Name the blood parasite species.
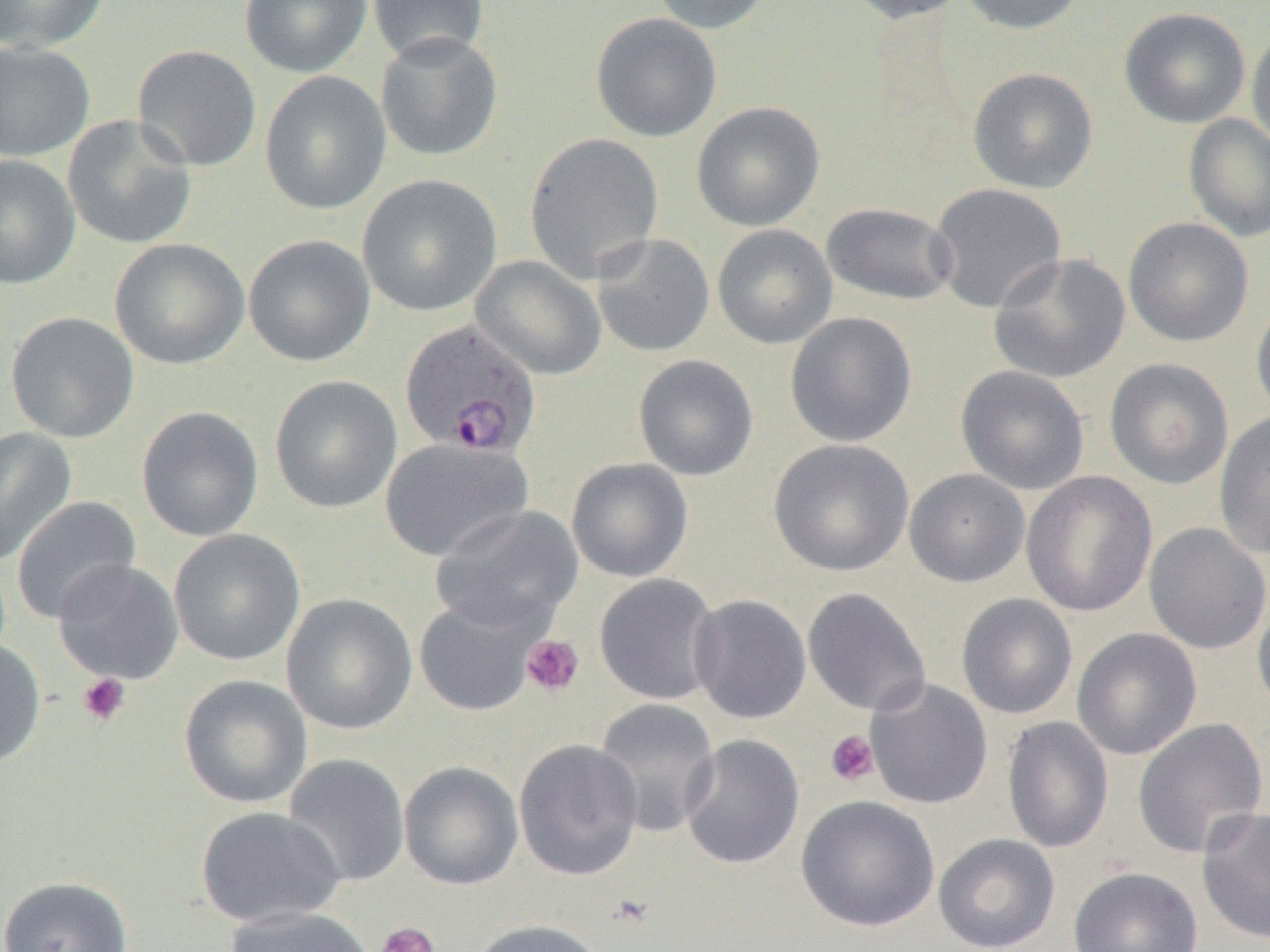
Plasmodium ovale.

Summary:
  - Coordinate format: approximate bounding boxes as (x1, y1, x2, y2) in pixels
  - Plasmodium ovale-infected red blood cell locations: (399, 319, 543, 458)
  - Platelet locations: (521, 634, 584, 697), (77, 673, 131, 727), (825, 729, 879, 786), (608, 893, 654, 929), (374, 921, 441, 952)
  - Uninfected red blood cell locations: (0, 0, 109, 53), (239, 0, 372, 77), (365, 0, 491, 66), (648, 0, 772, 34), (841, 0, 973, 23), (955, 0, 1089, 35), (1119, 7, 1251, 129), (590, 12, 722, 142), (1246, 30, 1270, 153), (375, 31, 504, 162), (0, 42, 96, 161), (131, 44, 262, 173), (967, 67, 1098, 193), (260, 71, 392, 216), (691, 102, 825, 231), (1183, 113, 1270, 242), (62, 114, 198, 250), (524, 133, 664, 283), (0, 154, 81, 289), (357, 174, 501, 317), (928, 183, 1067, 313), (821, 202, 958, 306), (1122, 216, 1254, 347), (712, 224, 837, 349), (592, 233, 715, 357), (243, 234, 376, 367), (110, 238, 250, 370), (988, 252, 1131, 384), (470, 255, 607, 381), (1250, 296, 1270, 423), (785, 311, 918, 447), (6, 312, 140, 443), (633, 355, 759, 481), (1104, 358, 1234, 489), (956, 365, 1090, 495), (269, 375, 403, 514), (136, 406, 264, 542), (1214, 411, 1270, 559), (0, 427, 77, 565), (381, 437, 533, 563), (769, 439, 914, 577), (567, 457, 694, 583), (904, 469, 1030, 587), (1021, 471, 1157, 617), (10, 496, 142, 624), (430, 505, 584, 635), (1144, 522, 1270, 655), (168, 529, 306, 666), (52, 559, 184, 685), (594, 573, 722, 705), (802, 587, 932, 717), (1252, 589, 1270, 719), (281, 593, 418, 735), (956, 593, 1078, 719), (688, 594, 812, 724), (414, 595, 543, 717), (1072, 627, 1202, 760), (0, 636, 46, 768), (179, 674, 313, 809), (866, 678, 993, 810), (594, 698, 721, 838), (1002, 716, 1115, 853), (1132, 718, 1268, 859), (679, 733, 805, 870), (513, 738, 645, 881), (283, 753, 410, 887), (399, 761, 523, 890), (796, 795, 941, 932), (195, 805, 346, 928), (1196, 807, 1270, 944), (933, 833, 1061, 952), (1068, 866, 1204, 952), (0, 875, 134, 952), (223, 905, 379, 952), (469, 919, 608, 952)
  - Modality: optical microscopy
  - Image size: 1270×952 pixels
  - Magnification: 1000x
  - Preparation: thin blood film
  - Field of view: one of a larger specimen